Outline each blood parasite and name the species.
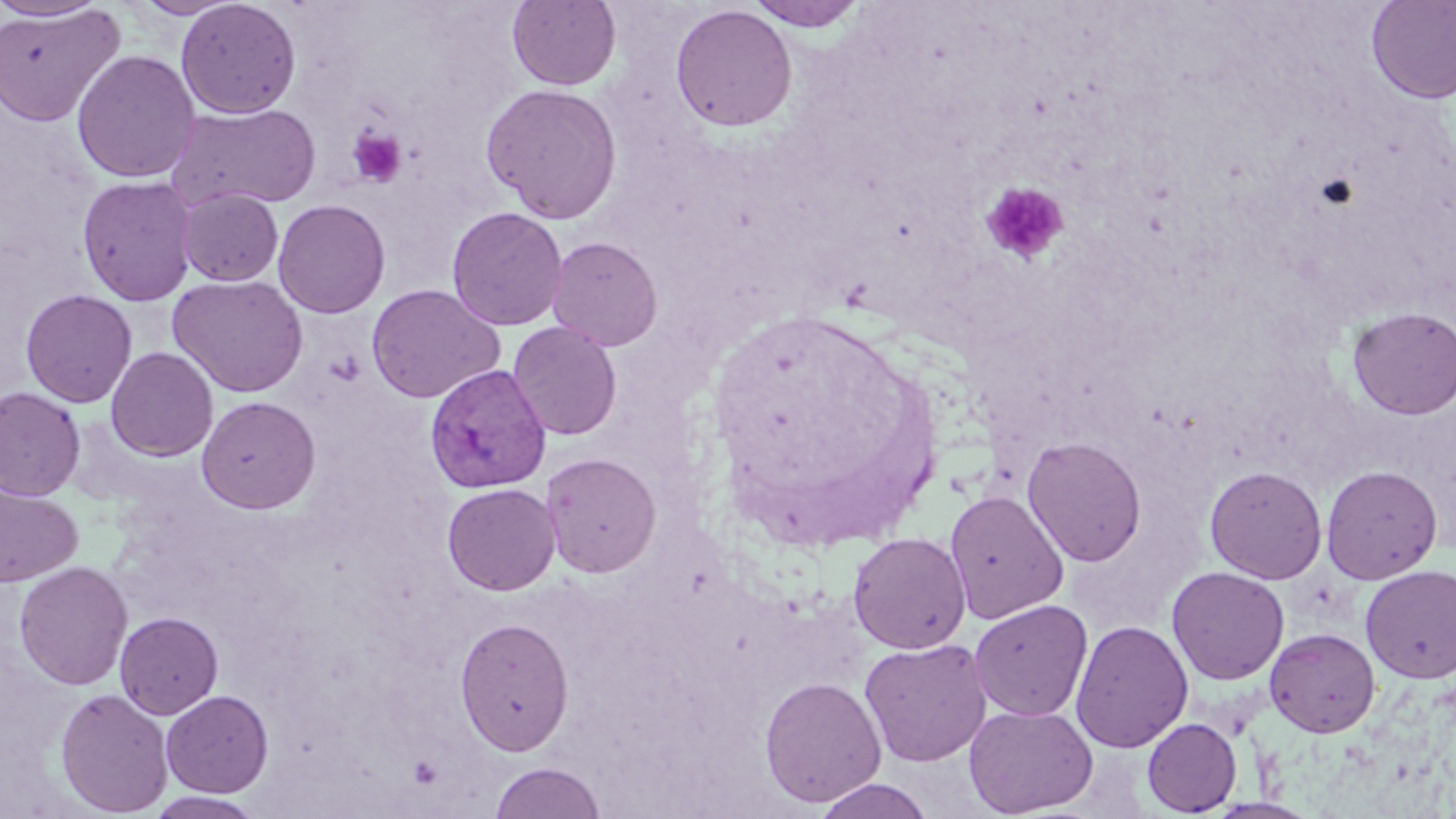
Approximate bounding boxes as [x1, y1, x2, y2] in pixels.
Plasmodium vivax-infected red blood cells: [424, 364, 551, 494].
No Plasmodium falciparum, Plasmodium ovale, Plasmodium malariae, Babesia divergens, or Trypanosoma brucei observed.

{
  "slide_level_diagnosis": "Plasmodium vivax",
  "uninfected_red_blood_cell_locations": "approximate bounding boxes as [x1, y1, x2, y2] in pixels: [0, 0, 113, 22], [131, 0, 240, 19], [176, 0, 302, 119], [507, 0, 622, 91], [745, 0, 868, 32], [1365, 0, 1456, 105], [669, 4, 797, 132], [0, 5, 124, 126], [71, 49, 200, 184], [480, 82, 622, 224], [167, 102, 322, 212], [76, 175, 199, 306], [176, 189, 284, 286], [272, 199, 390, 318], [446, 206, 568, 331], [547, 236, 663, 351], [168, 274, 309, 397], [366, 283, 505, 403], [20, 289, 137, 408], [1347, 306, 1456, 419], [507, 321, 623, 441], [105, 346, 219, 462], [0, 387, 85, 502], [196, 395, 321, 513], [1022, 436, 1147, 567], [542, 451, 661, 578], [1321, 464, 1442, 584], [1205, 465, 1328, 584], [441, 482, 561, 596], [1, 484, 83, 587], [944, 490, 1069, 623], [847, 531, 971, 654], [14, 561, 133, 690], [1360, 564, 1456, 683], [1166, 566, 1289, 685], [969, 599, 1093, 721], [114, 611, 223, 719], [454, 616, 574, 755], [1070, 619, 1193, 753], [1264, 627, 1381, 738], [859, 638, 992, 767], [759, 676, 886, 807], [55, 688, 173, 817], [161, 690, 273, 797], [963, 702, 1098, 817], [1142, 717, 1242, 816], [488, 761, 608, 819], [812, 778, 937, 819], [145, 792, 267, 818]",
  "platelet_locations": "approximate bounding boxes as [x1, y1, x2, y2] in pixels: [346, 125, 408, 188], [981, 181, 1070, 264]",
  "modality": "optical microscopy",
  "magnification": "1000x",
  "field_of_view": "one of a larger specimen",
  "preparation": "thin blood film",
  "stain": "May-Grünwald-Giemsa",
  "image_size": "1456×819 pixels"
}